Name the parasite shown.
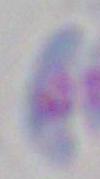
This is Toxoplasma gondii.

Micrograph. Captured at 1000x magnification.